Outline each blood parasite and name the species.
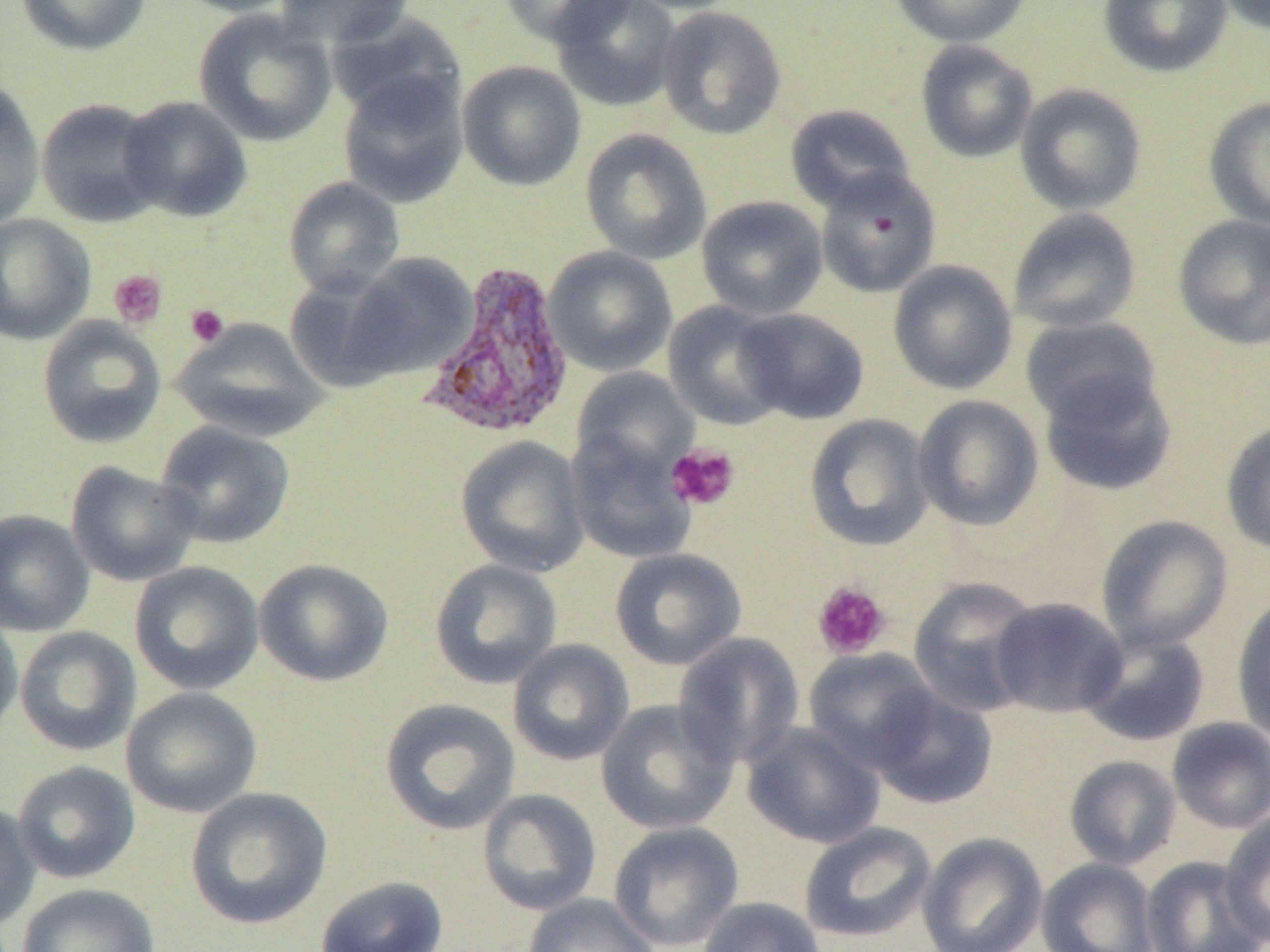
Approximate bounding boxes as named x1/y1/x2/y2 corners in pixels.
Plasmodium vivax-infected red blood cells: (x1=420, y1=261, x2=576, y2=440).
No Plasmodium falciparum, Plasmodium ovale, Plasmodium malariae, Babesia divergens, or Trypanosoma brucei observed.

Summary:
  - Platelet locations: (x1=108, y1=269, x2=167, y2=329), (x1=185, y1=304, x2=229, y2=347), (x1=666, y1=442, x2=741, y2=511), (x1=811, y1=580, x2=892, y2=660)
  - Uninfected red blood cell locations: (x1=15, y1=0, x2=152, y2=56), (x1=172, y1=0, x2=300, y2=17), (x1=275, y1=0, x2=413, y2=49), (x1=497, y1=0, x2=636, y2=47), (x1=551, y1=0, x2=681, y2=112), (x1=622, y1=0, x2=747, y2=14), (x1=889, y1=0, x2=1033, y2=48), (x1=1098, y1=0, x2=1233, y2=78), (x1=1216, y1=0, x2=1269, y2=35), (x1=656, y1=5, x2=787, y2=139), (x1=193, y1=10, x2=338, y2=147), (x1=325, y1=12, x2=465, y2=122), (x1=915, y1=40, x2=1038, y2=163), (x1=457, y1=60, x2=587, y2=191), (x1=337, y1=70, x2=469, y2=208), (x1=0, y1=77, x2=46, y2=230), (x1=1015, y1=83, x2=1147, y2=215), (x1=118, y1=96, x2=251, y2=222), (x1=1203, y1=96, x2=1270, y2=229), (x1=35, y1=98, x2=165, y2=227), (x1=784, y1=104, x2=917, y2=213), (x1=580, y1=128, x2=712, y2=265), (x1=815, y1=166, x2=942, y2=298), (x1=283, y1=177, x2=405, y2=298), (x1=696, y1=196, x2=828, y2=320), (x1=1007, y1=207, x2=1142, y2=334), (x1=0, y1=214, x2=96, y2=345), (x1=1172, y1=214, x2=1270, y2=350), (x1=543, y1=246, x2=678, y2=377), (x1=343, y1=253, x2=477, y2=380), (x1=888, y1=260, x2=1018, y2=395), (x1=283, y1=273, x2=408, y2=391), (x1=662, y1=301, x2=791, y2=431), (x1=733, y1=308, x2=870, y2=425), (x1=37, y1=316, x2=166, y2=449), (x1=1019, y1=316, x2=1162, y2=426), (x1=171, y1=318, x2=329, y2=442), (x1=1037, y1=366, x2=1178, y2=496), (x1=571, y1=367, x2=698, y2=478), (x1=911, y1=395, x2=1045, y2=532), (x1=803, y1=413, x2=935, y2=552), (x1=1221, y1=420, x2=1270, y2=556), (x1=155, y1=421, x2=296, y2=549), (x1=566, y1=428, x2=697, y2=565), (x1=455, y1=435, x2=589, y2=577), (x1=65, y1=461, x2=200, y2=587), (x1=0, y1=509, x2=94, y2=636), (x1=1096, y1=515, x2=1233, y2=653), (x1=609, y1=547, x2=747, y2=670), (x1=253, y1=558, x2=394, y2=686), (x1=429, y1=559, x2=563, y2=689), (x1=129, y1=561, x2=264, y2=695), (x1=908, y1=576, x2=1043, y2=717), (x1=1231, y1=592, x2=1270, y2=744), (x1=990, y1=597, x2=1128, y2=718), (x1=0, y1=606, x2=23, y2=743), (x1=15, y1=626, x2=141, y2=756), (x1=1080, y1=628, x2=1210, y2=747), (x1=672, y1=632, x2=805, y2=769), (x1=507, y1=638, x2=635, y2=766), (x1=803, y1=647, x2=940, y2=773), (x1=121, y1=687, x2=263, y2=818), (x1=869, y1=688, x2=999, y2=811), (x1=379, y1=698, x2=521, y2=835), (x1=595, y1=699, x2=738, y2=835), (x1=1166, y1=717, x2=1270, y2=834), (x1=743, y1=722, x2=885, y2=848), (x1=1064, y1=755, x2=1182, y2=870), (x1=12, y1=760, x2=141, y2=885), (x1=185, y1=786, x2=333, y2=930), (x1=477, y1=788, x2=602, y2=916), (x1=0, y1=801, x2=40, y2=933), (x1=1219, y1=811, x2=1270, y2=948), (x1=608, y1=820, x2=745, y2=951), (x1=798, y1=821, x2=936, y2=943), (x1=917, y1=832, x2=1048, y2=952), (x1=1140, y1=856, x2=1268, y2=952), (x1=1036, y1=857, x2=1159, y2=952), (x1=315, y1=875, x2=449, y2=952), (x1=17, y1=882, x2=160, y2=952), (x1=522, y1=893, x2=660, y2=952), (x1=695, y1=896, x2=827, y2=952)
  - Slide-level diagnosis: Plasmodium vivax
  - Image size: 1270×952 pixels
  - Modality: light microscopy
  - Preparation: thin blood smear
  - Field of view: single
  - Magnification: 1000x